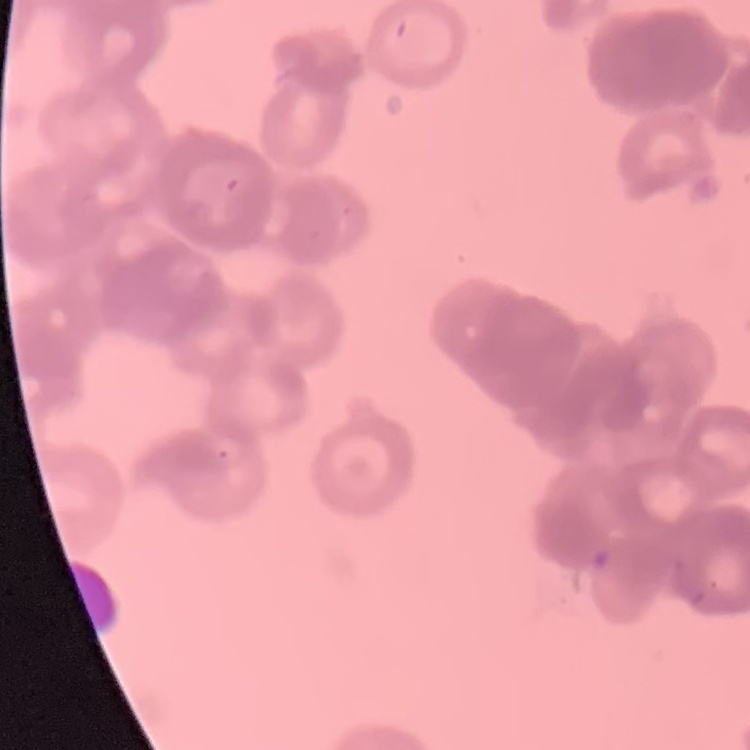
Summary:
  - Red blood cell morphology: rouleaux formation
  - Preparation: thin blood film
  - Stain: Field's or Giemsa
  - Image type: one tile cut from a larger photomicrograph